Locate every Plasmodium parasite.
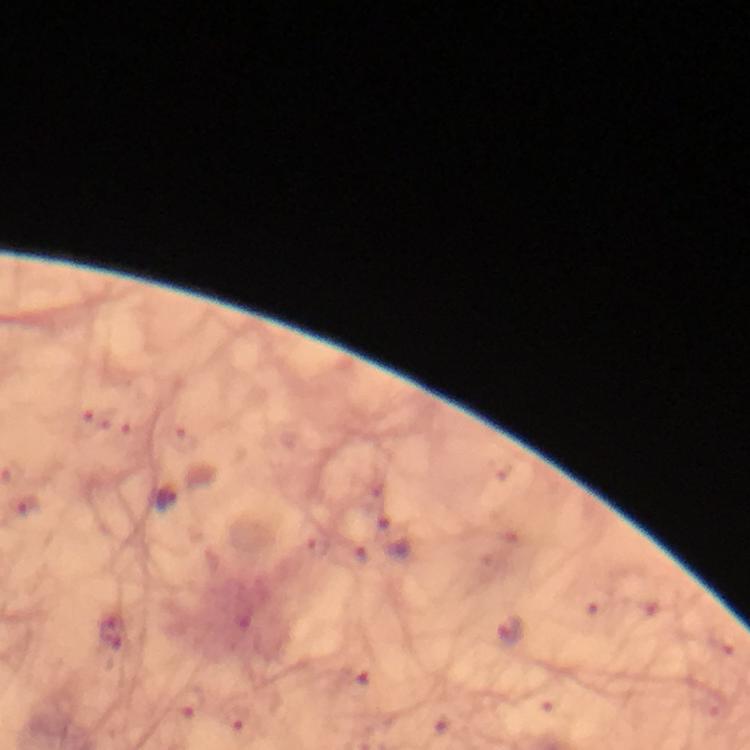

Approximate centers as (x, y) in pixels.
Plasmodium parasites: (167, 499), (512, 632).

Summary:
  - Cropped from: one field of view
  - Context: from a diagnostic examination for malaria
  - Image size: 750×750 pixels
  - Magnification: 100x
  - Stain: Giemsa
  - Preparation: thick smear
  - Capture: smartphone photograph through a microscope
  - Immersion oil: used